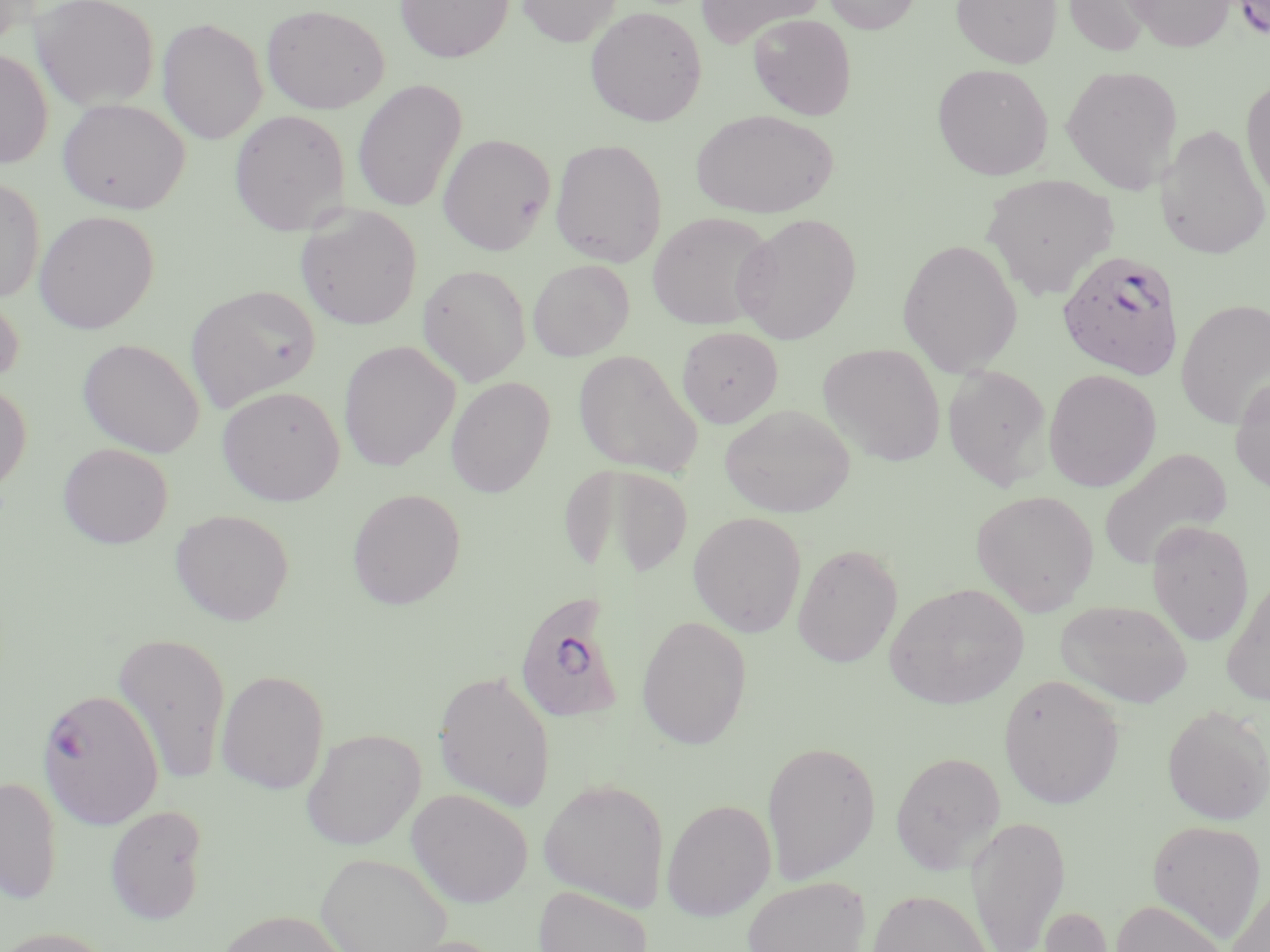

slide-level diagnosis = Plasmodium falciparum
modality = light microscopy
uninfected red blood cell locations = approximate bounding boxes as named x1/y1/x2/y2 corners in pixels: (x1=31, y1=0, x2=161, y2=111), (x1=395, y1=0, x2=514, y2=63), (x1=516, y1=0, x2=622, y2=47), (x1=696, y1=0, x2=826, y2=49), (x1=823, y1=0, x2=921, y2=34), (x1=951, y1=0, x2=1061, y2=67), (x1=1062, y1=0, x2=1153, y2=55), (x1=1126, y1=0, x2=1234, y2=51), (x1=1230, y1=0, x2=1270, y2=40), (x1=261, y1=3, x2=390, y2=114), (x1=585, y1=6, x2=707, y2=126), (x1=748, y1=14, x2=857, y2=120), (x1=157, y1=17, x2=268, y2=144), (x1=0, y1=49, x2=53, y2=169), (x1=932, y1=63, x2=1053, y2=180), (x1=1061, y1=64, x2=1183, y2=194), (x1=1240, y1=75, x2=1270, y2=209), (x1=352, y1=79, x2=467, y2=213), (x1=58, y1=98, x2=190, y2=214), (x1=228, y1=109, x2=351, y2=235), (x1=691, y1=109, x2=839, y2=218), (x1=1157, y1=124, x2=1270, y2=259), (x1=437, y1=133, x2=556, y2=255), (x1=549, y1=138, x2=668, y2=267), (x1=981, y1=174, x2=1119, y2=299), (x1=0, y1=177, x2=45, y2=302), (x1=295, y1=206, x2=423, y2=330), (x1=33, y1=210, x2=159, y2=334), (x1=647, y1=212, x2=776, y2=330), (x1=732, y1=213, x2=861, y2=344), (x1=896, y1=238, x2=1023, y2=377), (x1=528, y1=259, x2=634, y2=361), (x1=417, y1=263, x2=532, y2=386), (x1=185, y1=285, x2=320, y2=411), (x1=0, y1=289, x2=25, y2=389), (x1=1176, y1=299, x2=1270, y2=429), (x1=677, y1=325, x2=783, y2=427), (x1=77, y1=338, x2=204, y2=457), (x1=338, y1=340, x2=460, y2=471), (x1=818, y1=343, x2=946, y2=466), (x1=573, y1=349, x2=702, y2=477), (x1=942, y1=364, x2=1053, y2=491), (x1=1043, y1=369, x2=1162, y2=492), (x1=1230, y1=375, x2=1270, y2=494), (x1=445, y1=377, x2=555, y2=497), (x1=0, y1=381, x2=31, y2=495), (x1=217, y1=385, x2=346, y2=506), (x1=719, y1=404, x2=856, y2=518), (x1=57, y1=442, x2=173, y2=549), (x1=1098, y1=448, x2=1233, y2=569), (x1=560, y1=463, x2=693, y2=580), (x1=347, y1=488, x2=466, y2=609), (x1=970, y1=489, x2=1100, y2=615), (x1=170, y1=508, x2=294, y2=625), (x1=688, y1=511, x2=807, y2=637), (x1=1146, y1=519, x2=1255, y2=646), (x1=792, y1=543, x2=903, y2=668), (x1=1221, y1=574, x2=1270, y2=705), (x1=884, y1=582, x2=1029, y2=710), (x1=1055, y1=599, x2=1193, y2=708), (x1=636, y1=615, x2=753, y2=749), (x1=112, y1=631, x2=231, y2=786), (x1=433, y1=669, x2=556, y2=811), (x1=216, y1=670, x2=330, y2=794), (x1=998, y1=674, x2=1124, y2=809), (x1=1162, y1=705, x2=1270, y2=824), (x1=301, y1=728, x2=425, y2=850), (x1=761, y1=739, x2=881, y2=884), (x1=890, y1=751, x2=1006, y2=874), (x1=0, y1=776, x2=63, y2=904), (x1=538, y1=778, x2=669, y2=912), (x1=406, y1=788, x2=534, y2=907), (x1=662, y1=798, x2=776, y2=921), (x1=104, y1=805, x2=209, y2=924), (x1=965, y1=814, x2=1071, y2=952), (x1=1147, y1=819, x2=1267, y2=941), (x1=315, y1=852, x2=453, y2=952), (x1=741, y1=875, x2=871, y2=952), (x1=1225, y1=881, x2=1270, y2=952), (x1=533, y1=885, x2=653, y2=952), (x1=867, y1=888, x2=995, y2=951), (x1=1112, y1=899, x2=1228, y2=952), (x1=1038, y1=905, x2=1117, y2=952), (x1=215, y1=910, x2=352, y2=952), (x1=0, y1=926, x2=117, y2=952)
preparation = thin blood film
Plasmodium falciparum-infected red blood cell locations = approximate bounding boxes as named x1/y1/x2/y2 corners in pixels: (x1=1058, y1=249, x2=1185, y2=380), (x1=512, y1=591, x2=628, y2=725), (x1=36, y1=687, x2=164, y2=830)
field of view = single
magnification = 1000x
stain = May-Grünwald-Giemsa
image size = 1270×952 pixels